Report the malaria status of this cell.
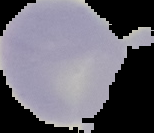

It is uninfected.

image size = 154×133 pixels
image type = segmented cell region with the area outside set to black
preparation = thin blood film